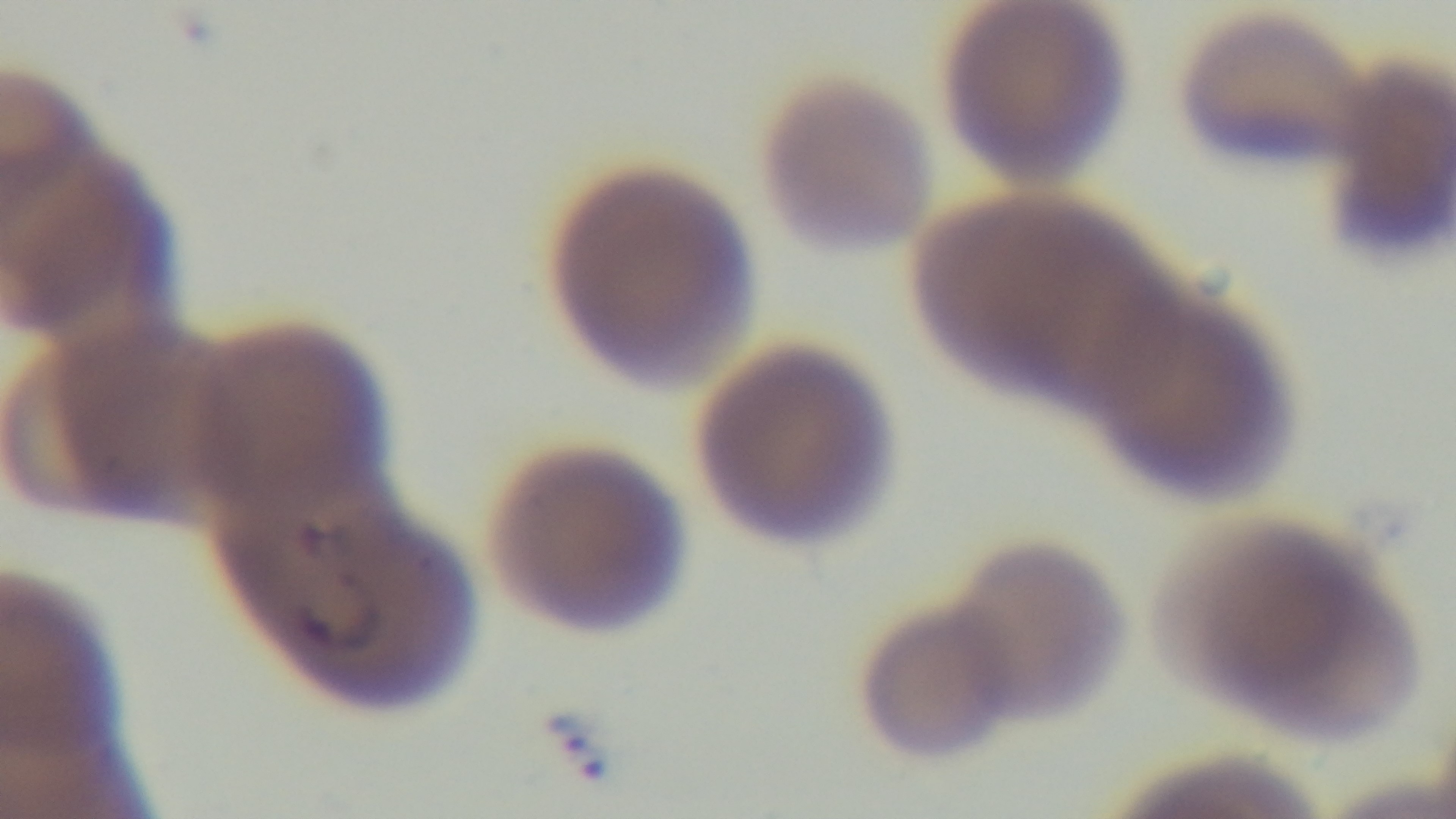
stain = Giemsa
modality = light microscopy
preparation = thin smear
field of view = one from the slide
capture = mounted 4K digital camera
objective = 100x oil immersion
malaria status = infected